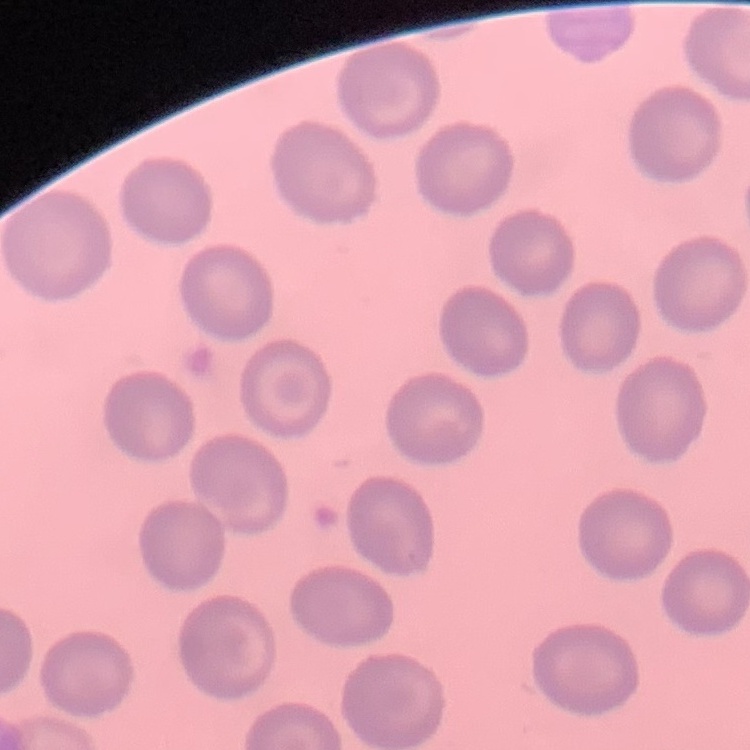

erythrocyte morphology = no rouleaux formation
preparation = thin blood smear
stain = Field's or Giemsa
image type = square crop of a larger photomicrograph